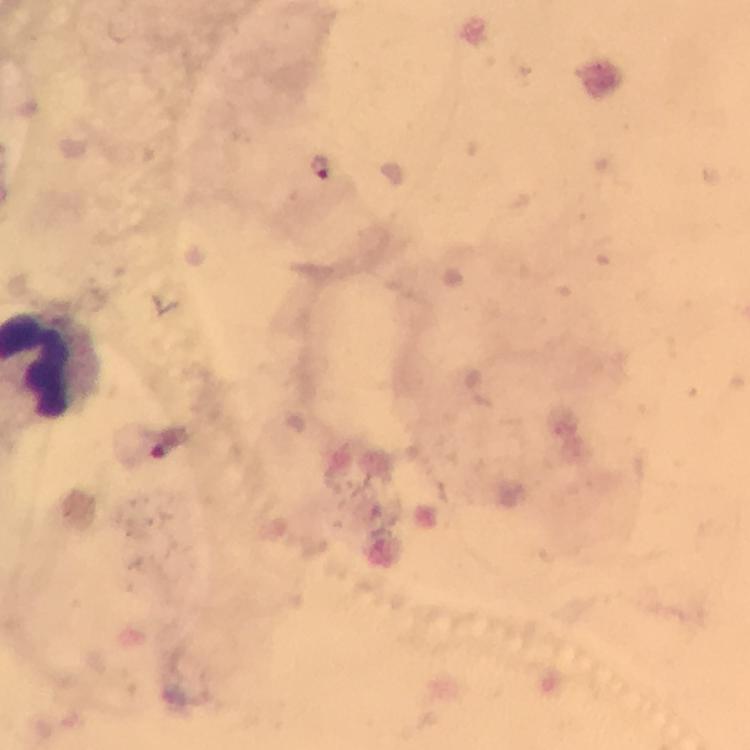

Approximate centers as [x, y] in pixels.
Summary:
  - Plasmodium parasite locations: [321, 168]
  - Immersion oil: applied
  - Context: from a malaria diagnostic workup
  - Magnification: 100x
  - Capture: smartphone photograph through a microscope
  - Preparation: thick smear
  - Stain: Giemsa
  - Image size: 750×750 pixels
  - Cropped from: a single field of view